Evaluate for Plasmodium parasites.
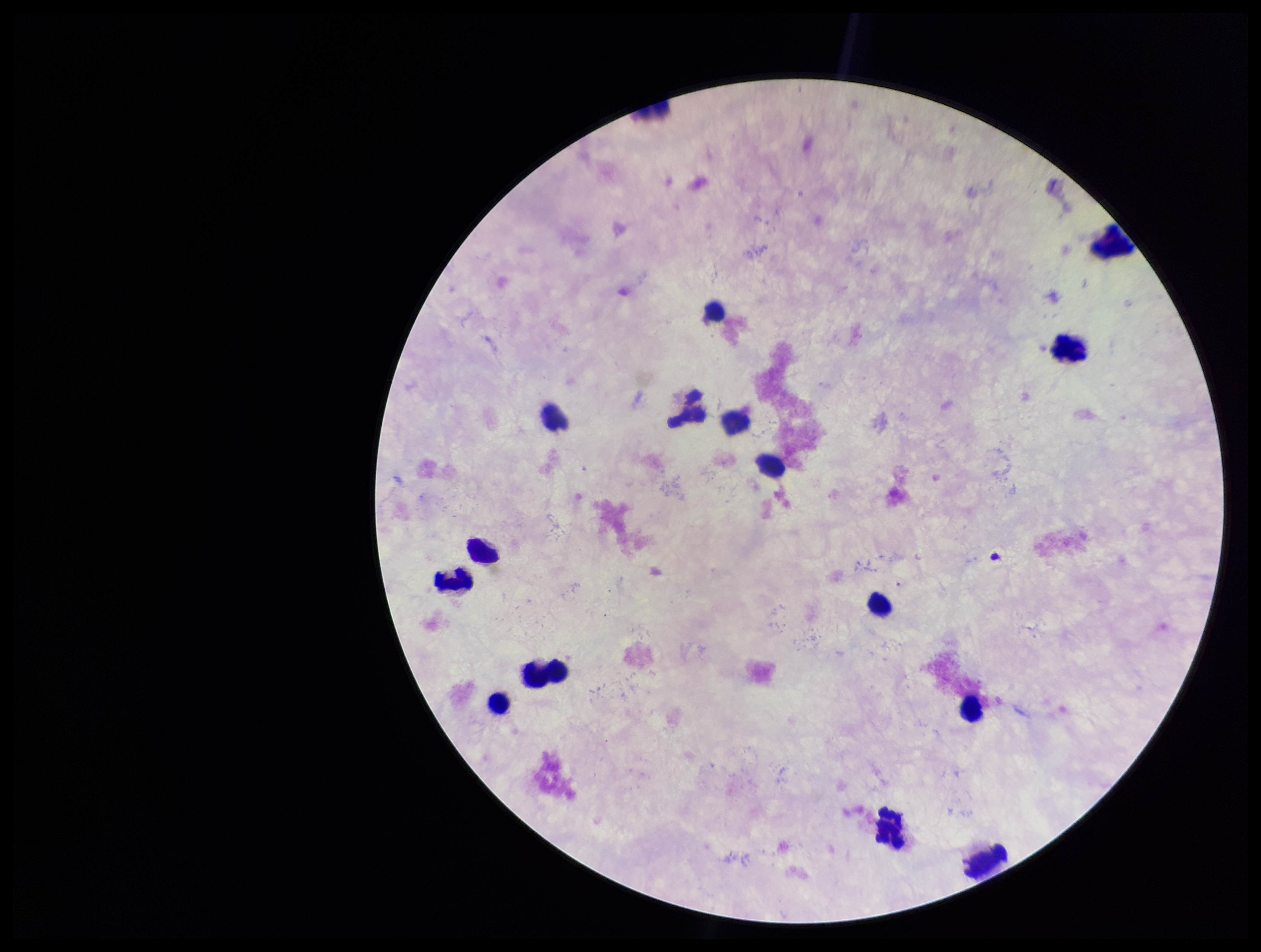

None identified.

image size = 1261×952 pixels
leukocyte count = 15
field of view = one from this slide
parasite count = 0
stain = Giemsa
capture = smartphone photograph through the microscope eyepiece
preparation = thick
patient malaria status = negative